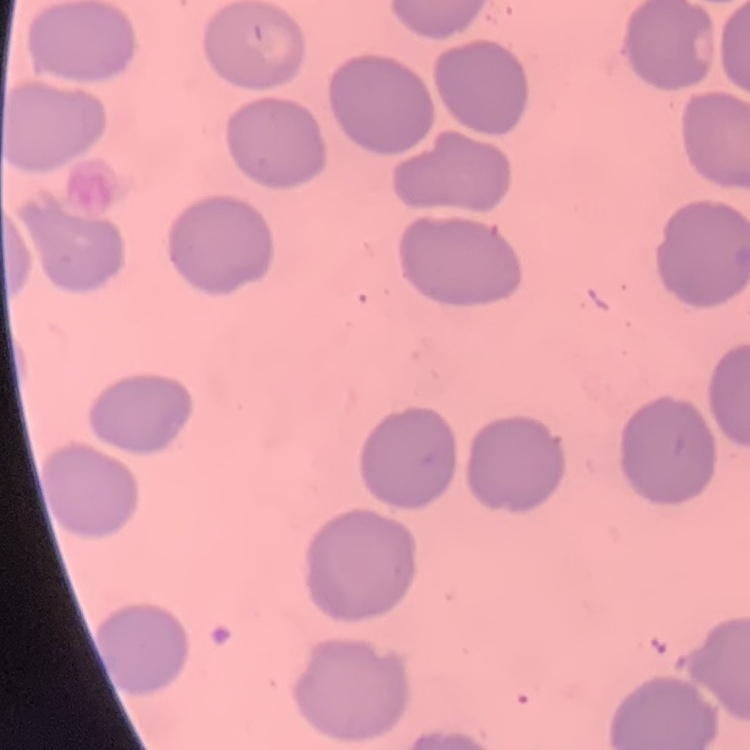
Summary:
  - Erythrocyte morphology: no rouleaux formation
  - Preparation: thin blood smear
  - Stain: Field's or Giemsa
  - Image type: one tile cut from a larger photomicrograph